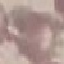
result = negative for malaria parasites
stain = Giemsa
image type = cell patch, automatically extracted from a larger field of view and resized to 64 × 64 pixels
preparation = thin smear
capture = smartphone camera at the microscope eyepiece